Locate every malaria parasite.
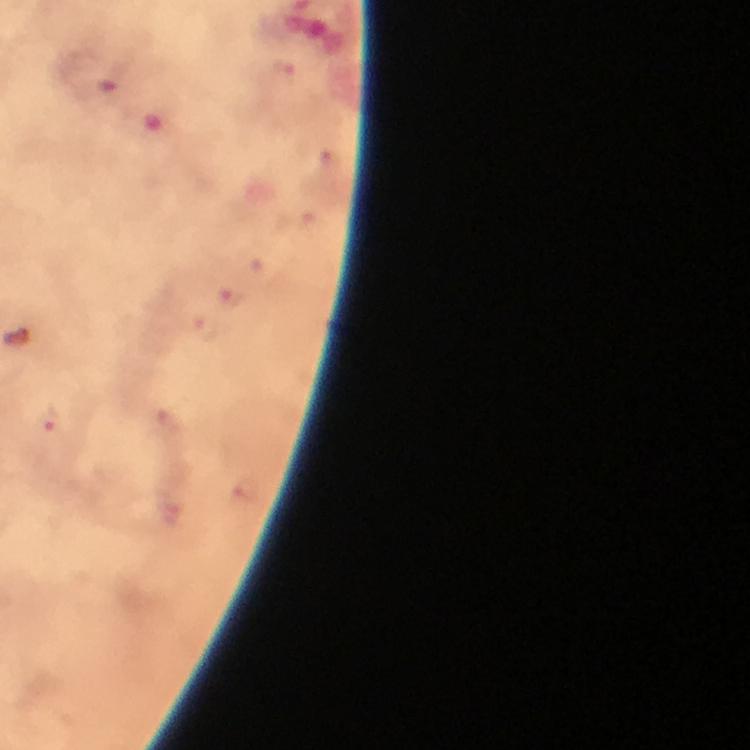

Approximate centers as (x, y) in pixels.
Malaria parasites: (231, 297), (204, 329), (50, 418).

Summary:
  - Capture: smartphone camera through the microscope
  - Immersion oil: used
  - Context: from a diagnostic examination for malaria
  - Preparation: thick smear
  - Cropped from: a single field of view
  - Image size: 750×750 pixels
  - Magnification: 100x
  - Stain: Giemsa